Assess this cell for malaria.
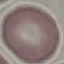

It is uninfected.

{
  "preparation": "thin blood film",
  "image_type": "cell patch, automatically extracted from a larger field of view and resized to 64 × 64 pixels",
  "stain": "Giemsa",
  "capture": "smartphone camera at the microscope eyepiece"
}